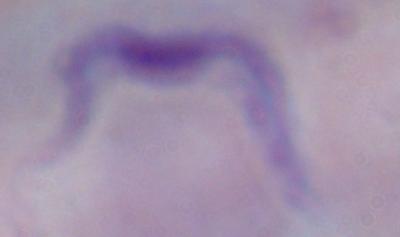

Summary:
  - Identification: trypanosome
  - Modality: micrograph
  - Magnification: 1000x